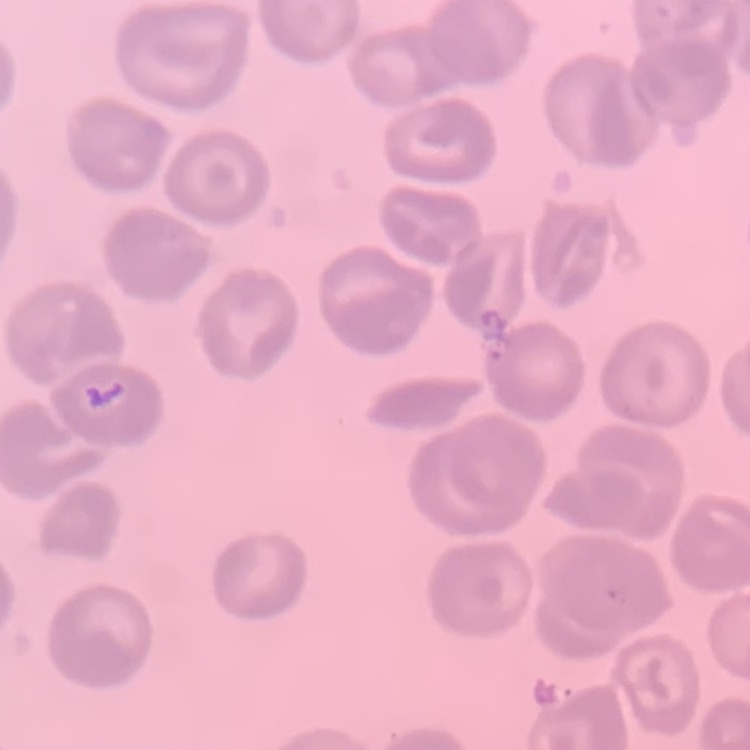
Summary:
  - Red blood cell morphology: no rouleaux formation
  - Preparation: thin blood smear
  - Stain: Field's or Giemsa
  - Image type: square crop of a larger photomicrograph